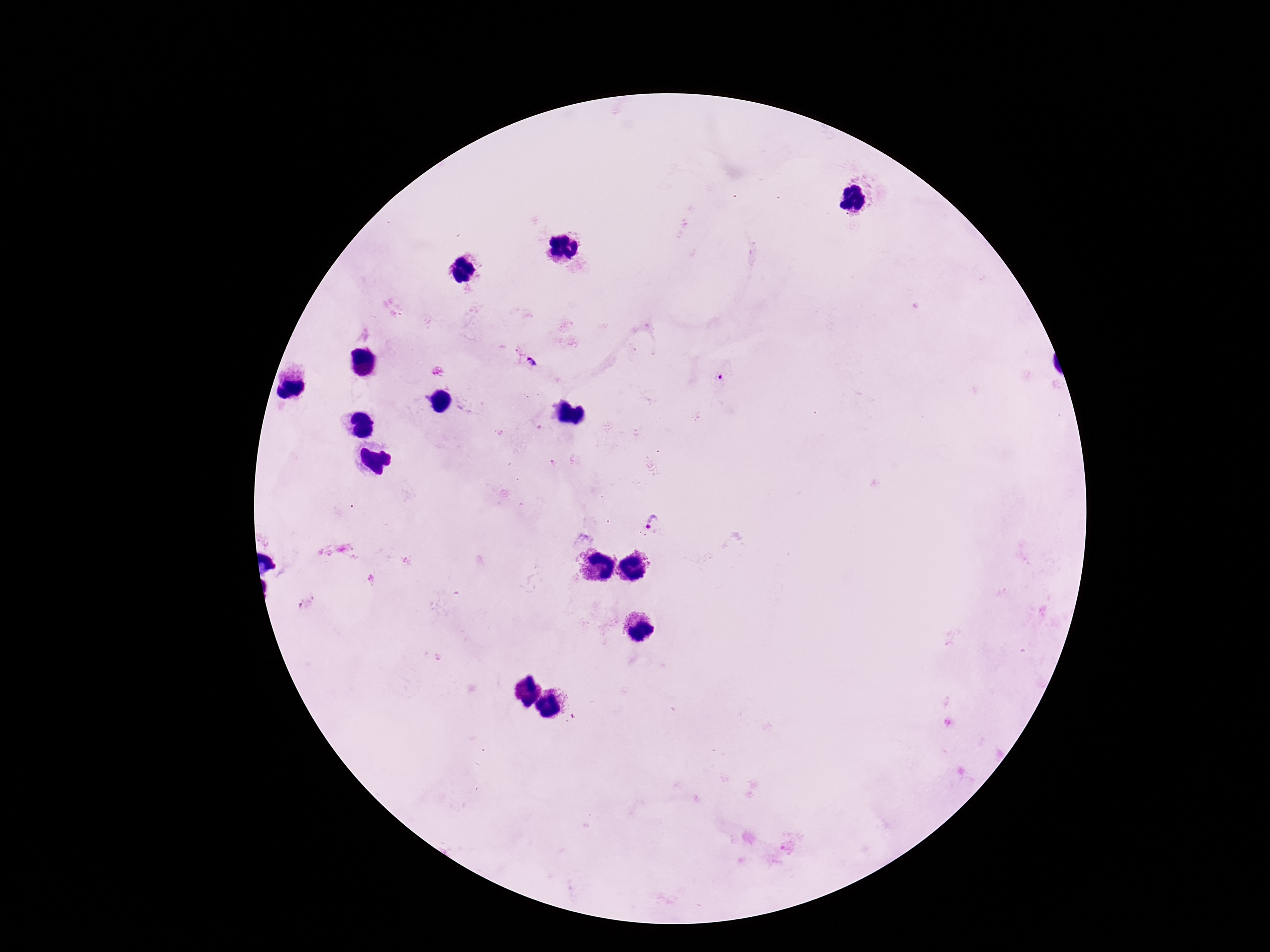
Approximate centers as (x, y) in pixels.
Summary:
  - Plasmodium parasite locations: (534, 364), (718, 378), (655, 524)
  - Stain: Giemsa
  - Preparation: thick blood smear
  - Image size: 1270×952 pixels
  - Capture: smartphone camera through the microscope eyepiece
  - Patient malaria status: positive
  - Field of view: single
  - Magnification: 100x